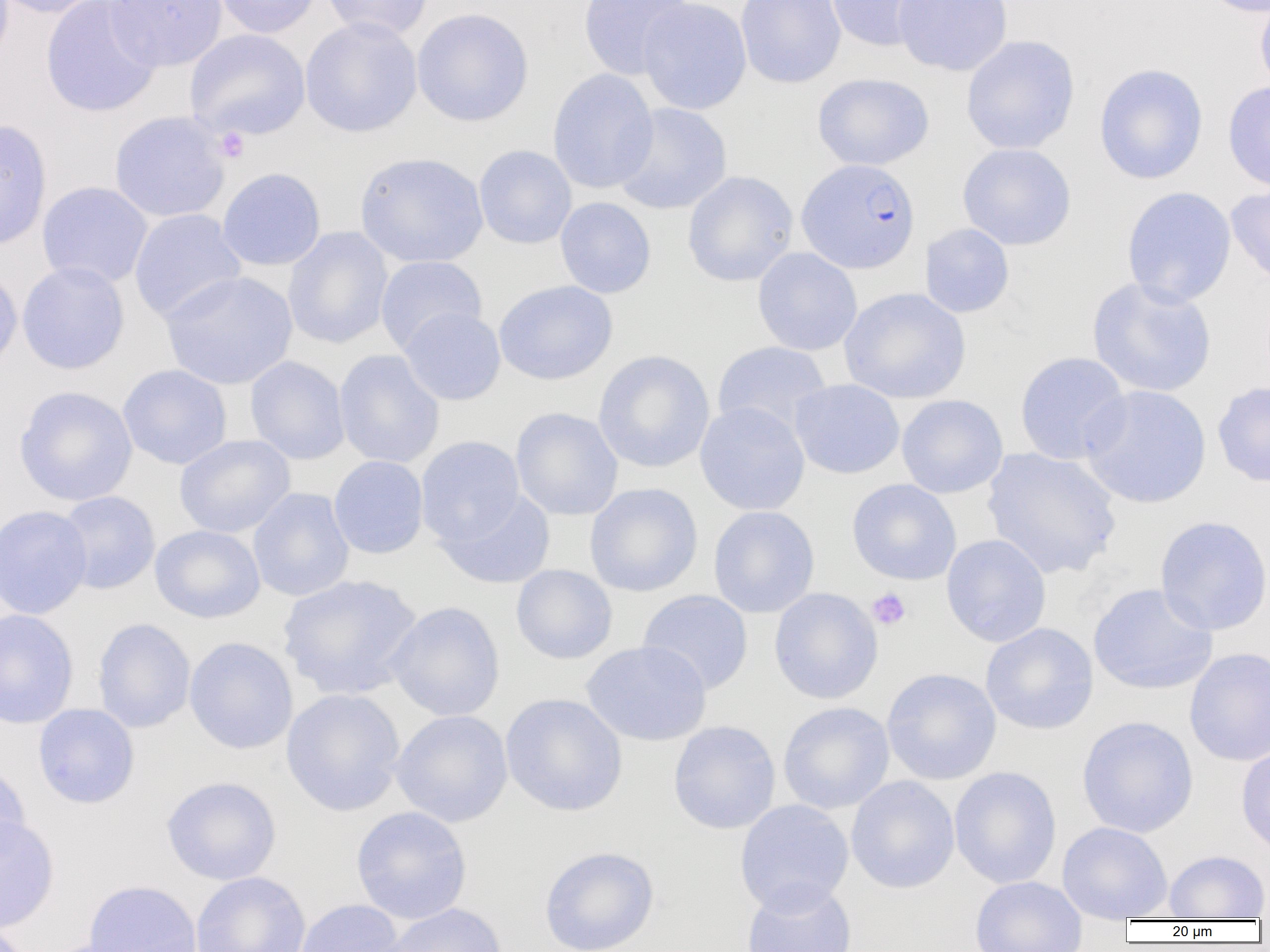 Approximate bounding boxes as named x1/y1/x2/y2 corners in pixels. Platelet locations: (x1=214, y1=127, x2=250, y2=162), (x1=866, y1=588, x2=911, y2=631). Uninfected red blood cell locations: (x1=0, y1=0, x2=111, y2=18), (x1=104, y1=0, x2=228, y2=71), (x1=213, y1=0, x2=322, y2=38), (x1=320, y1=0, x2=434, y2=41), (x1=577, y1=0, x2=694, y2=80), (x1=637, y1=0, x2=753, y2=115), (x1=736, y1=0, x2=846, y2=89), (x1=824, y1=0, x2=937, y2=52), (x1=891, y1=0, x2=1013, y2=77), (x1=1198, y1=0, x2=1269, y2=17), (x1=1255, y1=0, x2=1270, y2=98), (x1=41, y1=1, x2=162, y2=118), (x1=412, y1=8, x2=534, y2=127), (x1=300, y1=16, x2=422, y2=138), (x1=184, y1=28, x2=310, y2=141), (x1=960, y1=35, x2=1080, y2=155), (x1=1094, y1=62, x2=1209, y2=185), (x1=548, y1=68, x2=658, y2=194), (x1=812, y1=72, x2=934, y2=171), (x1=1222, y1=81, x2=1270, y2=193), (x1=611, y1=102, x2=733, y2=215), (x1=108, y1=111, x2=231, y2=223), (x1=0, y1=118, x2=52, y2=252), (x1=957, y1=143, x2=1076, y2=251), (x1=473, y1=145, x2=577, y2=249), (x1=355, y1=152, x2=488, y2=268), (x1=216, y1=167, x2=326, y2=271), (x1=682, y1=170, x2=799, y2=287), (x1=36, y1=181, x2=153, y2=289), (x1=1225, y1=184, x2=1270, y2=289), (x1=1121, y1=186, x2=1237, y2=308), (x1=555, y1=197, x2=656, y2=298), (x1=129, y1=209, x2=247, y2=323), (x1=920, y1=223, x2=1015, y2=318), (x1=283, y1=226, x2=393, y2=349), (x1=752, y1=247, x2=863, y2=356), (x1=375, y1=255, x2=487, y2=356), (x1=16, y1=261, x2=130, y2=375), (x1=0, y1=265, x2=23, y2=378), (x1=160, y1=271, x2=298, y2=390), (x1=1086, y1=276, x2=1217, y2=398), (x1=494, y1=280, x2=618, y2=385), (x1=839, y1=287, x2=971, y2=404), (x1=399, y1=307, x2=506, y2=405), (x1=712, y1=341, x2=832, y2=439), (x1=334, y1=349, x2=445, y2=469), (x1=593, y1=350, x2=715, y2=473), (x1=1015, y1=351, x2=1131, y2=465), (x1=245, y1=356, x2=350, y2=465), (x1=117, y1=364, x2=232, y2=469), (x1=789, y1=378, x2=905, y2=479), (x1=1212, y1=381, x2=1270, y2=487), (x1=13, y1=385, x2=138, y2=506), (x1=1079, y1=385, x2=1210, y2=508), (x1=897, y1=394, x2=1008, y2=498), (x1=695, y1=402, x2=810, y2=516), (x1=511, y1=407, x2=623, y2=521), (x1=174, y1=434, x2=295, y2=538), (x1=415, y1=436, x2=526, y2=546), (x1=982, y1=447, x2=1122, y2=580), (x1=328, y1=455, x2=429, y2=559), (x1=846, y1=479, x2=962, y2=585), (x1=584, y1=482, x2=703, y2=597), (x1=248, y1=487, x2=355, y2=602), (x1=436, y1=489, x2=556, y2=589), (x1=56, y1=491, x2=160, y2=595), (x1=0, y1=504, x2=93, y2=620), (x1=708, y1=506, x2=820, y2=618), (x1=1155, y1=515, x2=1270, y2=635), (x1=150, y1=524, x2=265, y2=623), (x1=941, y1=534, x2=1052, y2=647), (x1=511, y1=564, x2=618, y2=665), (x1=278, y1=574, x2=424, y2=700), (x1=1087, y1=582, x2=1218, y2=696), (x1=769, y1=588, x2=883, y2=704), (x1=637, y1=589, x2=754, y2=695), (x1=385, y1=601, x2=505, y2=721), (x1=0, y1=609, x2=79, y2=729), (x1=92, y1=618, x2=196, y2=733), (x1=980, y1=622, x2=1099, y2=735), (x1=184, y1=636, x2=298, y2=754), (x1=580, y1=640, x2=712, y2=747), (x1=1184, y1=647, x2=1270, y2=767), (x1=881, y1=667, x2=1002, y2=785), (x1=281, y1=688, x2=406, y2=816), (x1=500, y1=693, x2=628, y2=816), (x1=778, y1=701, x2=895, y2=814), (x1=33, y1=703, x2=140, y2=809), (x1=390, y1=709, x2=513, y2=827), (x1=1076, y1=715, x2=1199, y2=838), (x1=668, y1=720, x2=781, y2=834), (x1=1236, y1=742, x2=1270, y2=858), (x1=0, y1=761, x2=31, y2=867), (x1=949, y1=766, x2=1062, y2=889), (x1=846, y1=775, x2=960, y2=894), (x1=161, y1=776, x2=282, y2=885), (x1=734, y1=799, x2=853, y2=917), (x1=351, y1=805, x2=472, y2=924), (x1=0, y1=814, x2=60, y2=933), (x1=1057, y1=821, x2=1172, y2=921), (x1=539, y1=845, x2=660, y2=952), (x1=1164, y1=850, x2=1269, y2=920), (x1=190, y1=872, x2=311, y2=952), (x1=969, y1=875, x2=1087, y2=952), (x1=82, y1=879, x2=202, y2=952), (x1=741, y1=880, x2=857, y2=952), (x1=294, y1=899, x2=405, y2=952), (x1=377, y1=903, x2=508, y2=952). Plasmodium falciparum-infected red blood cell locations: (x1=797, y1=158, x2=920, y2=274). Slide-level diagnosis: Plasmodium falciparum. One field of a larger specimen. Captured at 1000x magnification. Thin blood film. Image is 1270×952 pixels. Light microscopy.